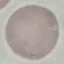

result = no malaria parasites seen
capture = smartphone camera at the microscope eyepiece
stain = Giemsa
preparation = thin blood smear
image type = cell patch, automatically extracted from a larger field of view and resized to 64 × 64 pixels